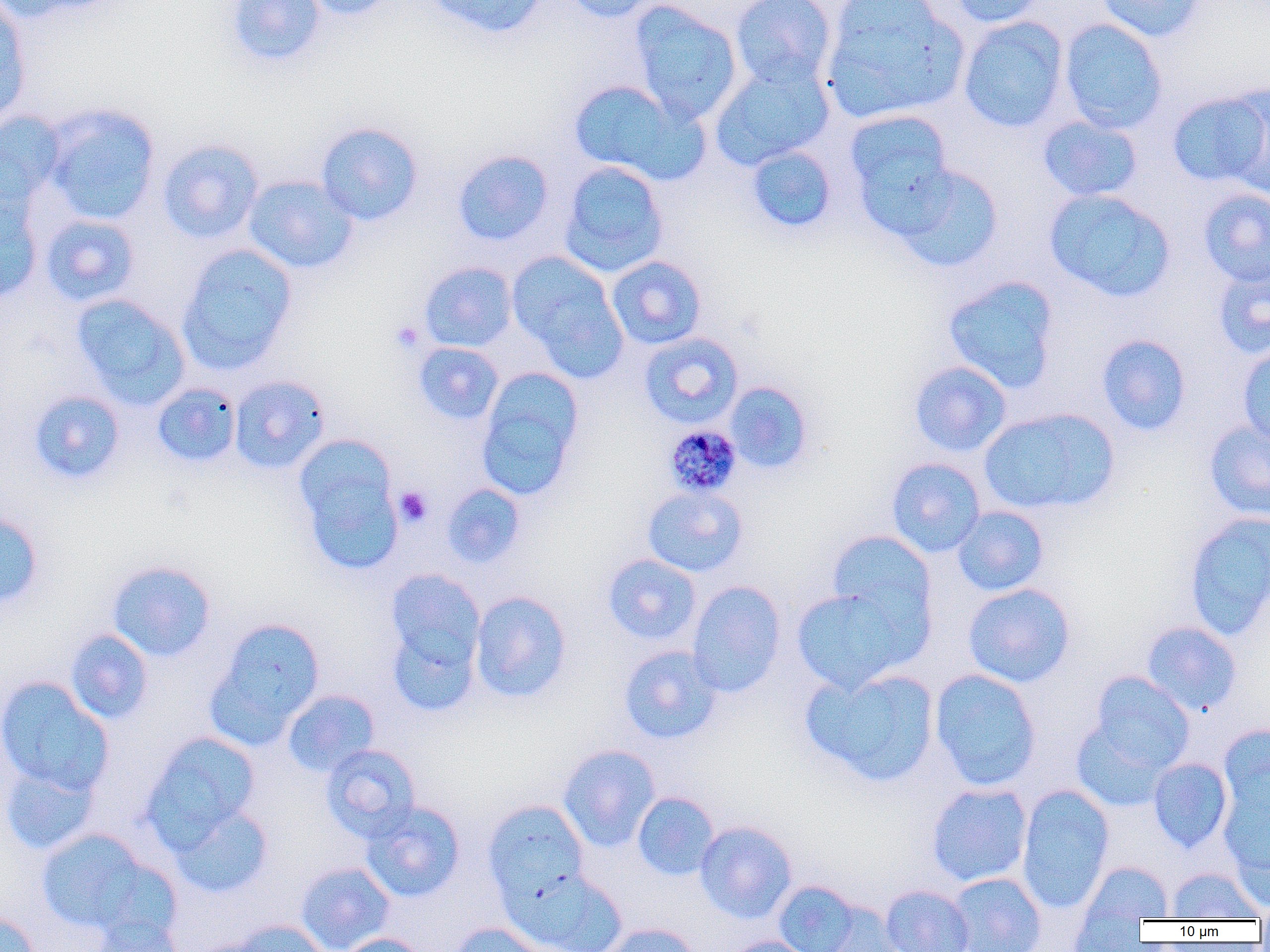
Summary:
  - Coordinate format: approximate bounding boxes as [x1, y1, x2, y2] in pixels
  - Uninfected red blood cell locations: [0, 0, 32, 124], [0, 0, 112, 22], [224, 0, 326, 67], [298, 0, 400, 20], [422, 0, 549, 39], [561, 0, 665, 24], [730, 0, 837, 90], [945, 0, 1047, 27], [1094, 0, 1207, 42], [820, 1, 968, 124], [628, 2, 742, 123], [958, 16, 1069, 133], [1059, 18, 1167, 133], [709, 63, 833, 171], [568, 79, 696, 181], [1220, 84, 1270, 198], [1167, 89, 1270, 190], [41, 103, 161, 225], [844, 109, 957, 230], [0, 110, 65, 211], [1037, 116, 1144, 202], [315, 121, 424, 226], [157, 138, 264, 243], [746, 145, 838, 234], [452, 149, 555, 247], [558, 160, 670, 277], [888, 162, 1004, 273], [243, 175, 358, 274], [0, 188, 44, 305], [1044, 188, 1176, 302], [1198, 188, 1270, 287], [40, 214, 141, 306], [177, 244, 298, 375], [506, 251, 626, 377], [606, 255, 707, 350], [419, 261, 518, 352], [1212, 262, 1270, 359], [941, 275, 1061, 394], [70, 293, 190, 409], [638, 332, 744, 429], [1096, 334, 1192, 436], [413, 342, 504, 425], [1236, 343, 1270, 448], [909, 360, 1012, 457], [475, 367, 584, 501], [229, 375, 331, 474], [723, 381, 814, 474], [152, 383, 241, 468], [28, 389, 126, 484], [979, 407, 1119, 516], [1203, 419, 1270, 522], [292, 434, 403, 572], [885, 457, 986, 558], [440, 483, 526, 569], [642, 485, 748, 577], [952, 505, 1050, 597], [0, 509, 45, 611], [1183, 510, 1270, 640], [826, 530, 936, 631], [602, 553, 702, 645], [106, 560, 217, 662], [385, 569, 485, 672], [686, 580, 787, 697], [963, 583, 1075, 687], [791, 586, 917, 693], [470, 590, 572, 703], [207, 617, 326, 744], [386, 621, 481, 717], [1141, 621, 1242, 715], [65, 629, 154, 724], [618, 645, 723, 745], [801, 666, 940, 787], [929, 668, 1042, 790], [1089, 671, 1195, 772], [0, 676, 114, 797], [282, 689, 380, 777], [1071, 718, 1173, 812], [1218, 723, 1269, 825], [142, 732, 261, 848], [321, 743, 421, 841], [558, 744, 661, 852], [1148, 757, 1233, 853], [0, 759, 100, 856], [926, 782, 1033, 886], [1220, 782, 1270, 897], [1016, 784, 1115, 913], [632, 791, 720, 880], [481, 799, 590, 906], [360, 801, 465, 902], [169, 803, 274, 899], [695, 820, 798, 923], [36, 827, 154, 934], [1079, 861, 1173, 924], [295, 862, 395, 951], [1166, 867, 1263, 921], [508, 868, 629, 952], [946, 872, 1046, 952], [772, 880, 864, 952], [880, 884, 975, 952], [819, 901, 905, 952], [1068, 910, 1149, 951], [0, 911, 42, 952], [87, 916, 184, 952], [226, 920, 331, 952], [447, 921, 551, 952], [601, 923, 702, 952], [337, 933, 429, 952], [718, 935, 819, 952]
  - Plasmodium malariae-infected red blood cell locations: [663, 424, 742, 498]
  - Platelet locations: [390, 321, 424, 354], [394, 486, 433, 527]
  - Slide-level diagnosis: Plasmodium malariae
  - Field of view: single
  - Image size: 1270×952 pixels
  - Preparation: thin blood smear
  - Modality: light microscopy
  - Magnification: 1000x